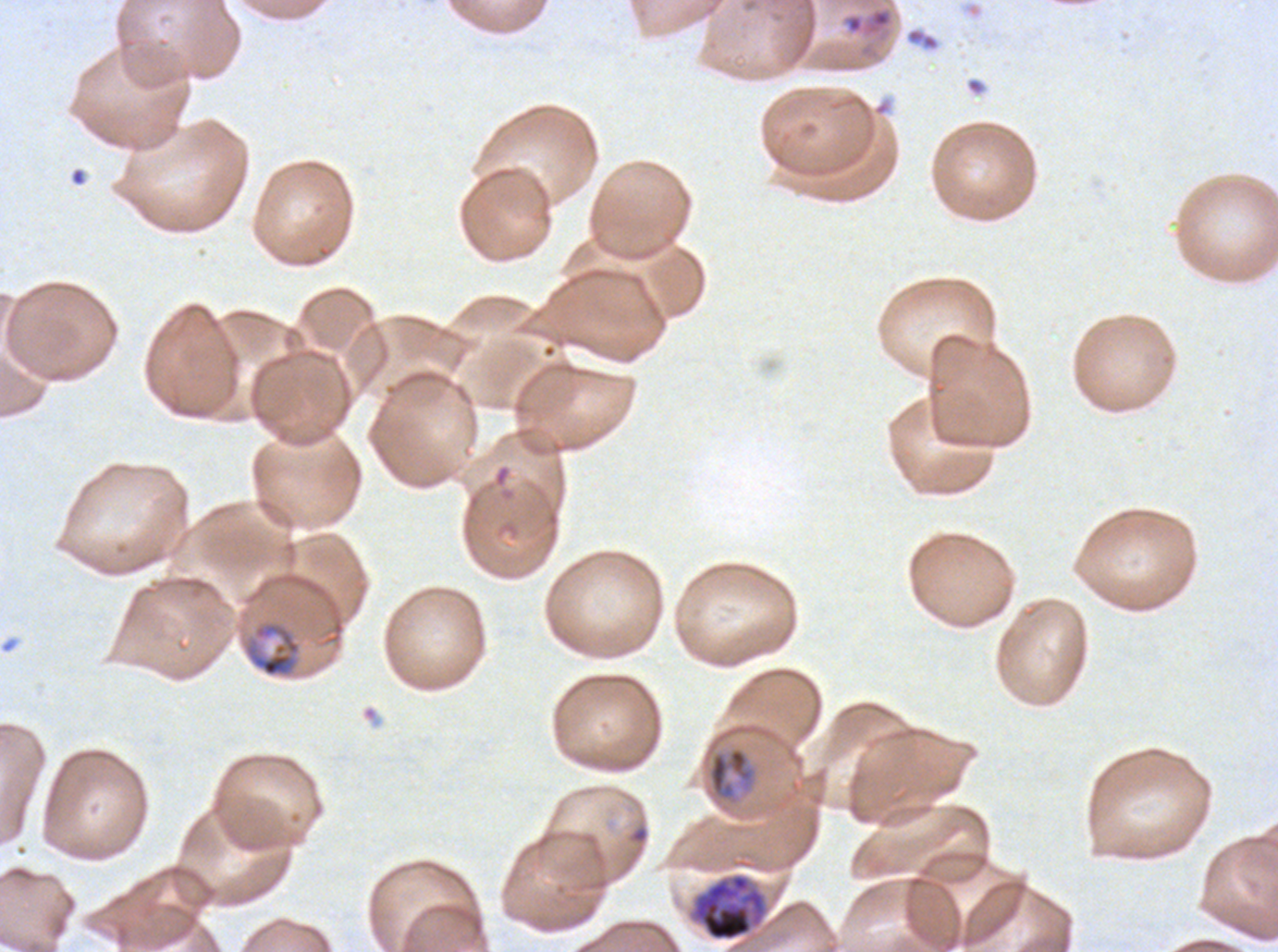

mid_trophozoite_locations: 'approximate bounding boxes as (x1, y1, x2, y2) in pixels: (242, 620, 301, 677), (707, 744, 758, 806)'
stain: Giemsa
image_size: 1278×952 pixels
life_cycle_stages_observed: ring, mid trophozoite, early schizont
debris_locations: 'approximate bounding boxes as (x1, y1, x2, y2) in pixels: (870, 9, 891, 28), (905, 28, 940, 51)'
ring_locations: 'approximate bounding boxes as (x1, y1, x2, y2) in pixels: (630, 825, 649, 845)'
field_of_view: one sub-image of a larger composite
preparation: thin blood film
specimen: P. falciparum from a patient in The Gambia, cultured ex vivo for 24 to 48 hours
early_schizont_locations: 'approximate bounding boxes as (x1, y1, x2, y2) in pixels: (692, 873, 766, 942)'